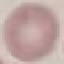

Summary:
  - Result: no malaria parasites detected
  - Capture: smartphone camera at the microscope eyepiece
  - Preparation: thin blood film
  - Image type: cell patch, automatically extracted from a larger field of view and resized to 64 × 64 pixels
  - Stain: Giemsa